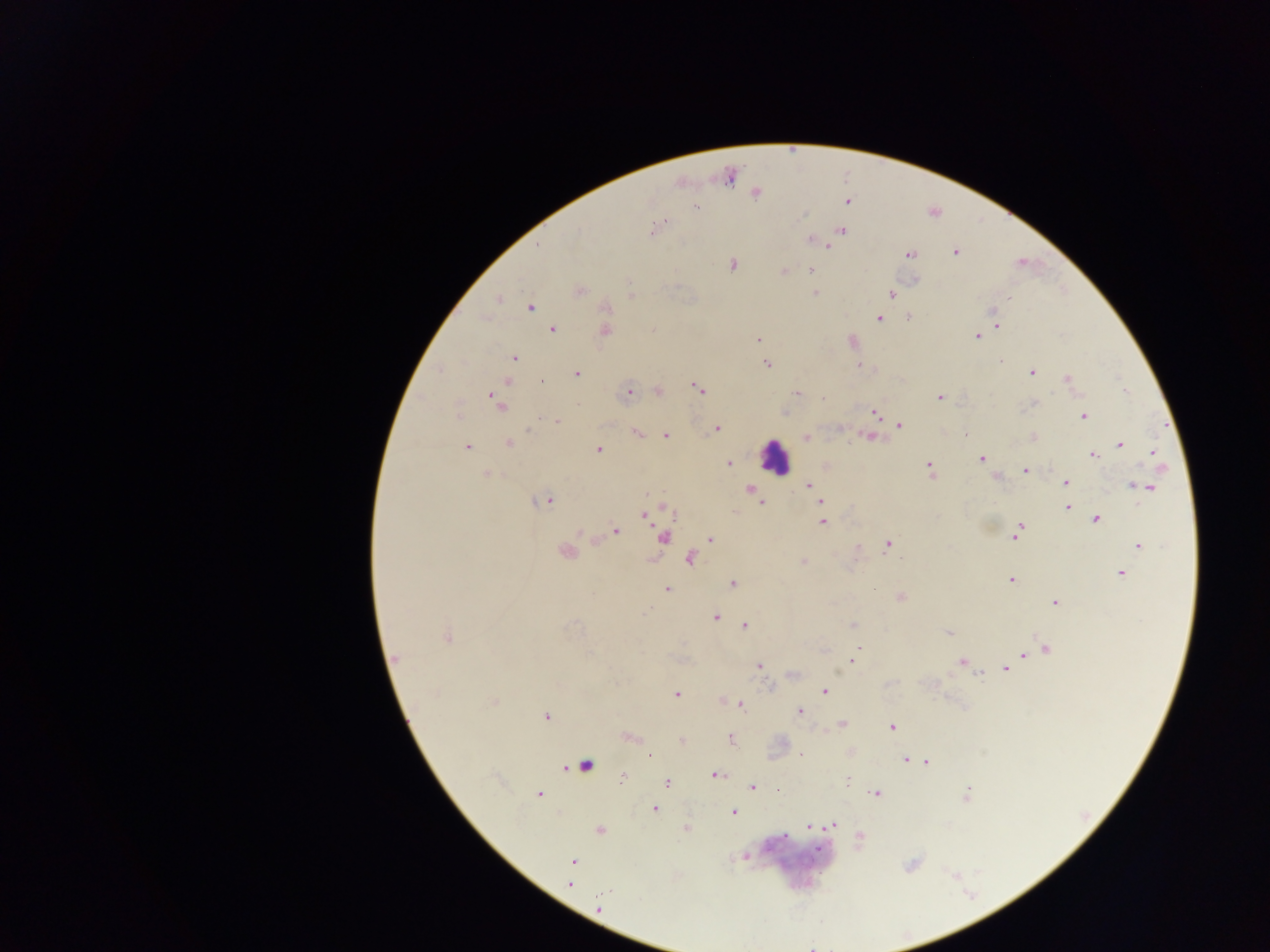

Approximate centers as {x, y} in pixels. Plasmodium parasite locations: {755, 193}, {847, 202}, {696, 207}, {803, 215}, {666, 220}, {661, 223}, {652, 231}, {841, 231}, {812, 240}, {822, 244}, {955, 253}, {910, 254}, {732, 264}, {783, 270}, {810, 270}, {915, 279}, {579, 290}, {815, 292}, {630, 294}, {891, 294}, {1008, 297}, {499, 299}, {1002, 301}, {530, 307}, {606, 308}, {993, 314}, {909, 318}, {878, 319}, {997, 325}, {553, 329}, {605, 330}, {978, 336}, {758, 339}, {852, 342}, {513, 358}, {766, 365}, {859, 365}, {1032, 372}, {576, 374}, {1068, 380}, {542, 382}, {697, 388}, {1125, 389}, {658, 390}, {627, 393}, {797, 394}, {939, 397}, {823, 398}, {496, 401}, {1034, 403}, {874, 413}, {1084, 416}, {556, 421}, {900, 425}, {529, 428}, {716, 429}, {636, 433}, {964, 434}, {666, 436}, {806, 436}, {869, 437}, {1034, 437}, {509, 443}, {1120, 444}, {467, 447}, {599, 450}, {1153, 453}, {1092, 454}, {981, 459}, {729, 463}, {929, 470}, {1025, 470}, {487, 475}, {996, 476}, {1065, 483}, {809, 485}, {1145, 487}, {750, 490}, {821, 501}, {544, 502}, {761, 503}, {1068, 507}, {645, 515}, {1096, 519}, {822, 522}, {616, 531}, {1016, 532}, {663, 537}, {711, 539}, {888, 545}, {1139, 546}, {565, 553}, {690, 559}, {803, 562}, {1121, 574}, {1011, 580}, {732, 584}, {668, 588}, {900, 596}, {1054, 603}, {648, 611}, {716, 617}, {853, 625}, {745, 626}, {948, 633}, {448, 637}, {859, 648}, {1046, 649}, {1024, 654}, {395, 659}, {853, 659}, {962, 662}, {759, 666}, {1006, 669}, {793, 674}, {980, 674}, {824, 691}, {676, 694}, {494, 702}, {740, 706}, {799, 712}, {546, 716}, {842, 724}, {892, 727}, {630, 736}, {731, 739}, {682, 740}, {650, 754}, {801, 754}, {906, 760}, {916, 761}, {927, 762}, {586, 765}, {716, 776}, {623, 777}, {847, 780}, {667, 784}, {752, 786}, {777, 790}, {966, 793}, {875, 794}, {539, 795}, {654, 809}, {732, 812}, {833, 825}, {810, 826}, {686, 829}, {600, 830}, {860, 836}, {744, 857}, {572, 861}, {569, 884}, {599, 909}. Leukocyte locations: {773, 457}. Collected in Ghana. Image is 1270×952 pixels. Mobile-phone photograph taken through the microscope. Single field of view. Thick blood film.